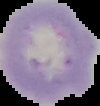

preparation = thin blood smear
image type = segmented cell region with the area outside set to black
result = no Plasmodium parasites detected
image size = 100×106 pixels